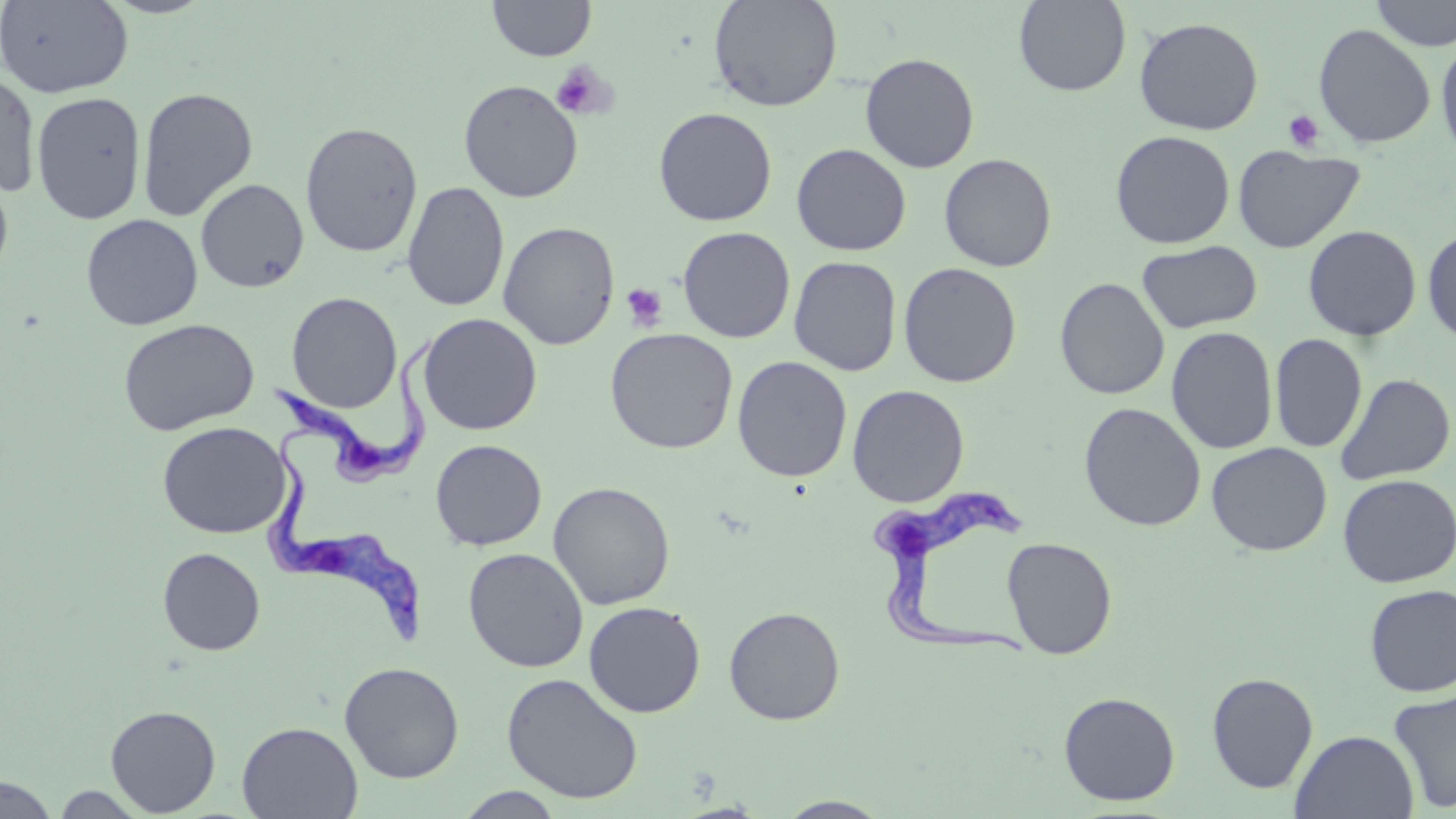

Approximate bounding boxes as named x1/y1/x2/y2 corners in pixels. Uninfected red blood cell locations: (x1=0, y1=0, x2=133, y2=98), (x1=487, y1=0, x2=597, y2=61), (x1=708, y1=0, x2=843, y2=113), (x1=1013, y1=0, x2=1131, y2=96), (x1=1370, y1=0, x2=1456, y2=51), (x1=1133, y1=16, x2=1264, y2=135), (x1=1313, y1=23, x2=1436, y2=148), (x1=1436, y1=36, x2=1456, y2=164), (x1=860, y1=52, x2=979, y2=173), (x1=0, y1=70, x2=41, y2=198), (x1=458, y1=79, x2=583, y2=203), (x1=137, y1=86, x2=258, y2=221), (x1=31, y1=91, x2=147, y2=224), (x1=653, y1=107, x2=777, y2=226), (x1=300, y1=122, x2=423, y2=258), (x1=1110, y1=130, x2=1235, y2=249), (x1=791, y1=143, x2=911, y2=256), (x1=1232, y1=144, x2=1365, y2=254), (x1=938, y1=153, x2=1057, y2=272), (x1=0, y1=166, x2=14, y2=283), (x1=196, y1=178, x2=309, y2=293), (x1=402, y1=181, x2=510, y2=312), (x1=80, y1=213, x2=203, y2=330), (x1=498, y1=221, x2=620, y2=350), (x1=1303, y1=224, x2=1422, y2=341), (x1=677, y1=226, x2=796, y2=343), (x1=1422, y1=226, x2=1456, y2=347), (x1=1137, y1=240, x2=1261, y2=333), (x1=789, y1=255, x2=902, y2=376), (x1=898, y1=262, x2=1022, y2=387), (x1=1054, y1=277, x2=1170, y2=400), (x1=286, y1=291, x2=403, y2=413), (x1=417, y1=313, x2=542, y2=435), (x1=117, y1=317, x2=259, y2=436), (x1=1166, y1=325, x2=1279, y2=454), (x1=604, y1=328, x2=739, y2=454), (x1=1270, y1=334, x2=1367, y2=452), (x1=732, y1=356, x2=852, y2=482), (x1=1335, y1=372, x2=1455, y2=486), (x1=847, y1=384, x2=969, y2=507), (x1=1079, y1=402, x2=1206, y2=531), (x1=157, y1=421, x2=291, y2=539), (x1=430, y1=439, x2=547, y2=551), (x1=1206, y1=441, x2=1332, y2=556), (x1=1337, y1=474, x2=1456, y2=588), (x1=548, y1=481, x2=676, y2=610), (x1=1002, y1=536, x2=1117, y2=658), (x1=157, y1=547, x2=265, y2=655), (x1=463, y1=547, x2=588, y2=672), (x1=1363, y1=584, x2=1456, y2=697), (x1=583, y1=601, x2=706, y2=718), (x1=723, y1=606, x2=845, y2=725), (x1=339, y1=661, x2=464, y2=783), (x1=501, y1=672, x2=644, y2=804), (x1=1206, y1=672, x2=1319, y2=793), (x1=1388, y1=687, x2=1456, y2=814), (x1=1058, y1=691, x2=1181, y2=806), (x1=105, y1=705, x2=221, y2=816), (x1=237, y1=721, x2=362, y2=818), (x1=1290, y1=730, x2=1419, y2=818), (x1=0, y1=775, x2=60, y2=819), (x1=49, y1=785, x2=153, y2=817), (x1=454, y1=787, x2=567, y2=818), (x1=774, y1=796, x2=894, y2=818). Trypanosoma brucei locations: (x1=267, y1=335, x2=441, y2=488), (x1=266, y1=432, x2=424, y2=649), (x1=867, y1=485, x2=1036, y2=659). Platelet locations: (x1=550, y1=61, x2=618, y2=121), (x1=1283, y1=110, x2=1326, y2=152), (x1=620, y1=282, x2=668, y2=331). Slide-level diagnosis: Trypanosoma brucei. One field of a larger specimen. Image is 1456×819 pixels. May-Grünwald-Giemsa stain. Optical microscopy. Thin blood film. Captured at 1000x magnification.